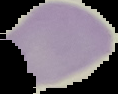
Image is 118×94 pixels. Result: no malaria parasites seen. Cell region segmented out of the field of view; the surrounding area is masked to black. From a thin blood film.